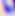
Micrograph. 400x magnification. Toxoplasma gondii is shown.